Name the blood parasite species.
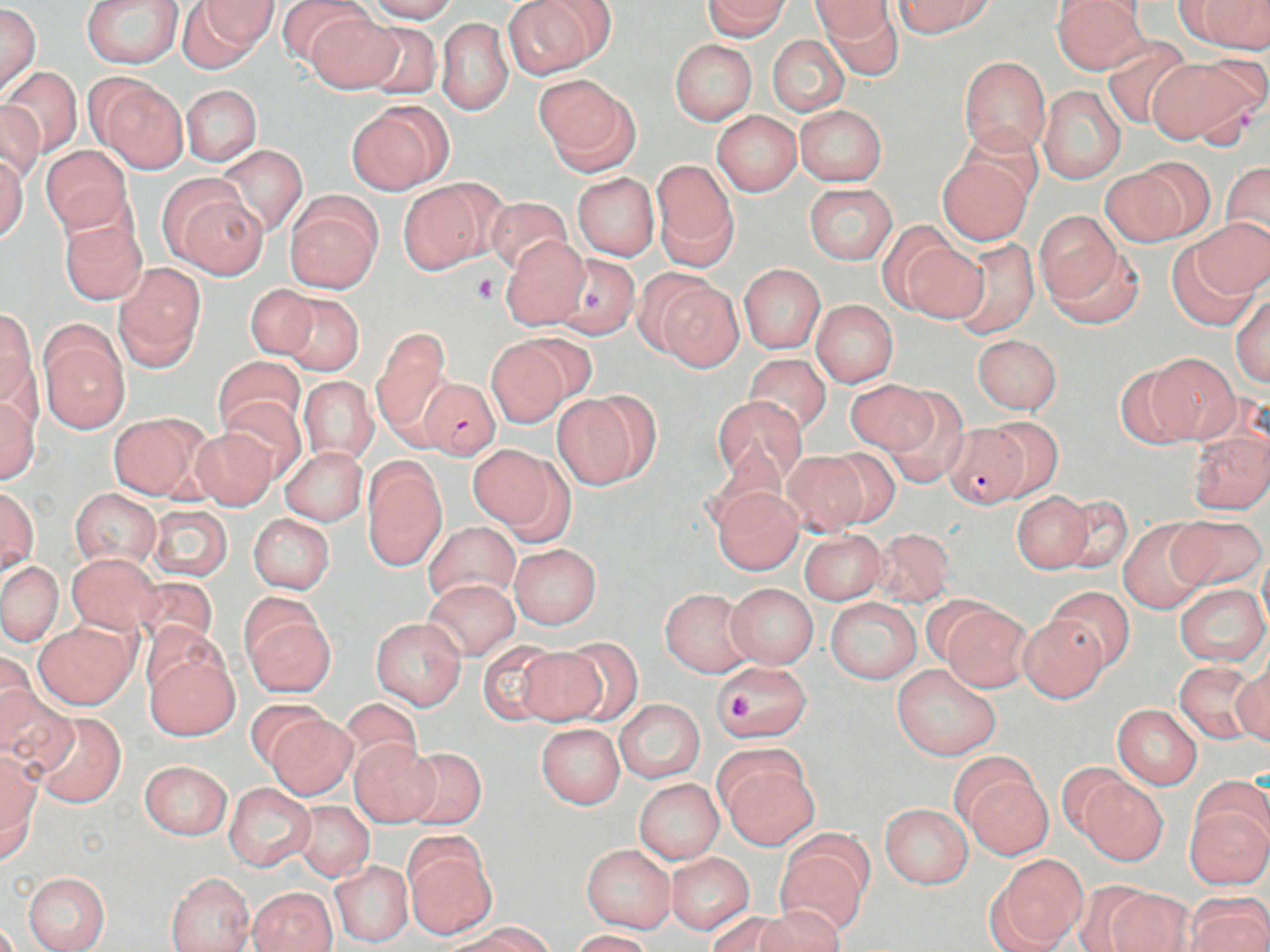
Plasmodium falciparum.

Approximate bounding boxes as [x1, y1, x2, y2] in pixels. Uninfected red blood cell locations: [81, 0, 185, 68], [179, 0, 275, 70], [276, 0, 370, 72], [367, 0, 458, 24], [505, 0, 611, 76], [702, 0, 790, 38], [893, 0, 992, 38], [1052, 0, 1148, 72], [1189, 0, 1268, 53], [808, 2, 896, 37], [817, 2, 902, 79], [0, 5, 41, 98], [305, 11, 403, 94], [437, 18, 513, 114], [355, 22, 445, 98], [767, 34, 849, 116], [1100, 35, 1194, 129], [670, 39, 757, 124], [959, 55, 1051, 156], [1145, 56, 1258, 145], [4, 66, 83, 158], [536, 74, 636, 170], [96, 79, 187, 172], [180, 84, 262, 165], [1037, 84, 1127, 183], [0, 99, 43, 183], [346, 101, 451, 194], [794, 105, 887, 185], [711, 111, 801, 196], [959, 124, 1044, 206], [214, 145, 309, 236], [41, 146, 132, 235], [0, 154, 27, 241], [938, 157, 1031, 244], [1127, 157, 1217, 239], [651, 162, 738, 269], [1222, 162, 1270, 246], [1100, 169, 1190, 247], [572, 173, 659, 260], [399, 180, 494, 271], [804, 182, 898, 265], [172, 191, 267, 280], [286, 192, 383, 294], [484, 196, 574, 275], [1034, 213, 1127, 307], [57, 217, 148, 305], [1194, 218, 1269, 297], [897, 235, 989, 323], [500, 236, 590, 330], [948, 237, 1039, 338], [1046, 242, 1145, 328], [1167, 244, 1260, 331], [555, 253, 637, 339], [113, 264, 206, 371], [739, 264, 825, 352], [654, 280, 745, 372], [244, 284, 320, 359], [273, 292, 364, 377], [1232, 294, 1269, 386], [810, 299, 898, 387], [0, 310, 36, 407], [39, 328, 128, 433], [374, 329, 452, 433], [972, 334, 1062, 414], [485, 338, 576, 427], [1144, 353, 1242, 444], [744, 354, 831, 436], [214, 356, 306, 439], [1112, 361, 1199, 448], [298, 376, 379, 463], [847, 379, 935, 453], [879, 390, 972, 485], [552, 392, 654, 489], [0, 395, 39, 486], [711, 396, 806, 489], [220, 397, 306, 483], [107, 411, 209, 500], [985, 416, 1064, 498], [942, 422, 1029, 509], [188, 426, 278, 510], [1187, 428, 1270, 515], [468, 444, 558, 528], [280, 446, 367, 525], [821, 448, 902, 527], [782, 452, 869, 535], [362, 457, 446, 568], [69, 486, 161, 568], [0, 487, 38, 572], [712, 487, 803, 573], [1009, 491, 1094, 574], [1056, 495, 1134, 574], [148, 504, 233, 579], [248, 514, 335, 594], [1170, 514, 1267, 590], [1118, 519, 1213, 613], [424, 521, 520, 606], [871, 528, 957, 606], [800, 529, 887, 603], [509, 543, 601, 629], [67, 553, 161, 634], [0, 560, 64, 647], [133, 577, 219, 653], [424, 580, 519, 660], [726, 582, 818, 667], [1174, 583, 1267, 665], [1045, 586, 1135, 672], [660, 588, 754, 676], [826, 597, 921, 684], [939, 601, 1034, 692], [240, 604, 336, 697], [1016, 616, 1108, 701], [371, 618, 466, 709], [33, 621, 138, 709], [560, 638, 644, 724], [478, 639, 566, 724], [513, 647, 607, 725], [146, 650, 239, 738], [0, 651, 37, 742], [1173, 659, 1261, 744], [711, 660, 815, 741], [1230, 663, 1270, 745], [890, 664, 1001, 761], [0, 688, 80, 779], [340, 697, 424, 774], [245, 699, 330, 771], [615, 699, 705, 783], [1113, 704, 1202, 789], [31, 710, 126, 807], [266, 714, 359, 801], [535, 723, 625, 808], [349, 740, 439, 826], [399, 747, 487, 830], [0, 753, 41, 861], [947, 753, 1038, 835], [718, 754, 819, 851], [139, 760, 231, 838], [1056, 761, 1132, 842], [962, 774, 1052, 858], [1078, 776, 1167, 865], [634, 779, 724, 864], [224, 783, 314, 869], [1183, 800, 1270, 890], [294, 802, 373, 881], [880, 803, 972, 888], [776, 836, 870, 934], [582, 844, 676, 933], [404, 846, 497, 938], [666, 852, 754, 933], [990, 854, 1088, 950], [330, 860, 412, 947], [22, 872, 110, 952], [166, 872, 254, 952], [1069, 879, 1161, 951], [1101, 887, 1196, 951], [248, 888, 337, 952], [1186, 894, 1270, 952], [754, 906, 846, 952], [706, 910, 793, 952], [454, 923, 554, 952], [568, 929, 654, 952]. Plasmodium falciparum-infected red blood cell locations: [417, 376, 501, 458]. Platelet locations: [472, 274, 500, 303], [728, 692, 755, 722]. Thin blood film. Captured at 1000x magnification. One field of a larger specimen. Optical microscopy. Image is 1270×952 pixels. May-Grünwald-Giemsa stain.